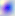
{
  "magnification": "400x",
  "identification": "Toxoplasma gondii",
  "modality": "photomicrograph"
}